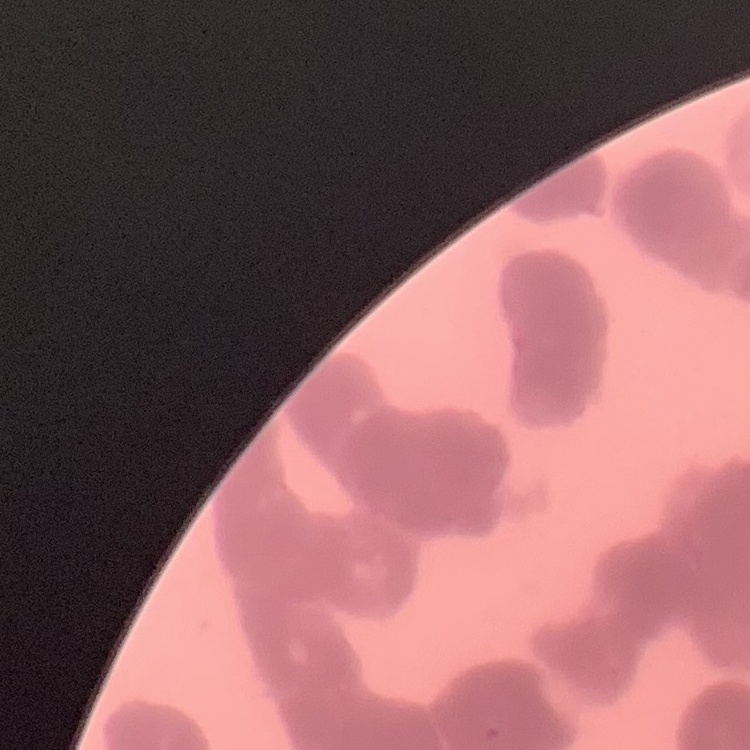
Summary:
  - Red blood cell morphology: rouleaux formation
  - Preparation: thin blood film
  - Image type: square crop of a larger photomicrograph
  - Stain: Field's or Giemsa